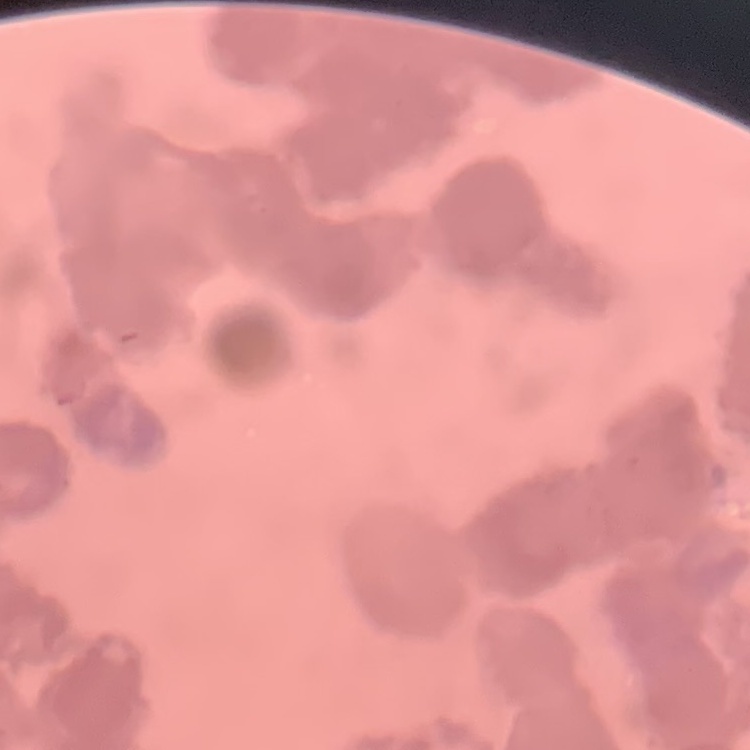

Summary:
  - Red blood cell morphology: rouleaux formation
  - Preparation: thin blood film
  - Image type: square crop of a larger photomicrograph
  - Stain: Field's or Giemsa